Classify this cell by malaria status.
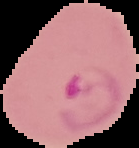
It is parasitized.

Summary:
  - Preparation: thin blood smear
  - Image type: segmented cell region with the area outside set to black
  - Image size: 139×148 pixels